Assess this cell for malaria.
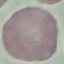
It is uninfected.

capture = smartphone camera at the microscope eyepiece
image type = cell patch, automatically extracted from a larger field of view and resized to 64 × 64 pixels
stain = Giemsa
preparation = thin smear